Assess this cell for malaria.
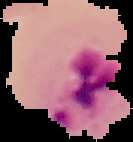

It is parasitized.

preparation = thin blood film
image type = cell region segmented out of the field of view; surrounding area masked to black
image size = 133×142 pixels